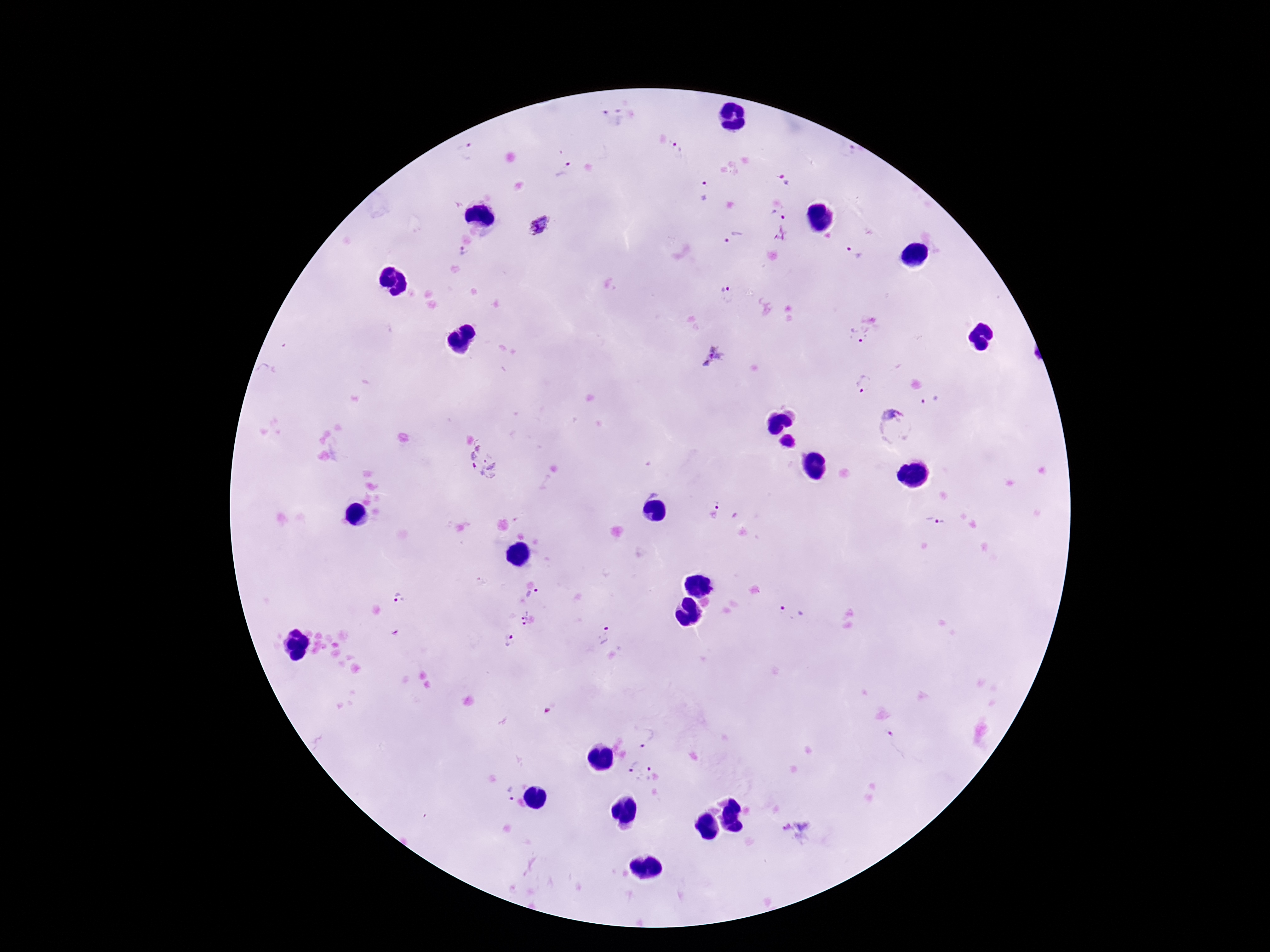
Approximate centers as [x, y] in pixels. Plasmodium parasite locations: [613, 118], [679, 150], [466, 152], [850, 152], [566, 171], [783, 180], [705, 191], [779, 214], [541, 227], [781, 235], [734, 239], [463, 252], [853, 253], [729, 294], [871, 318], [860, 334], [716, 359], [863, 383], [934, 400], [892, 429], [484, 459], [712, 508], [935, 522], [534, 595], [399, 600], [792, 615], [524, 618], [604, 636], [507, 641], [648, 737], [899, 744], [631, 765], [646, 775], [508, 792], [797, 831]. Patient malaria status: infected. 100x magnification. Thick blood film. Image is 1270×952 pixels. Single field of view. Giemsa stain. Smartphone photograph taken through the microscope eyepiece.